Outline each blood parasite and name the species.
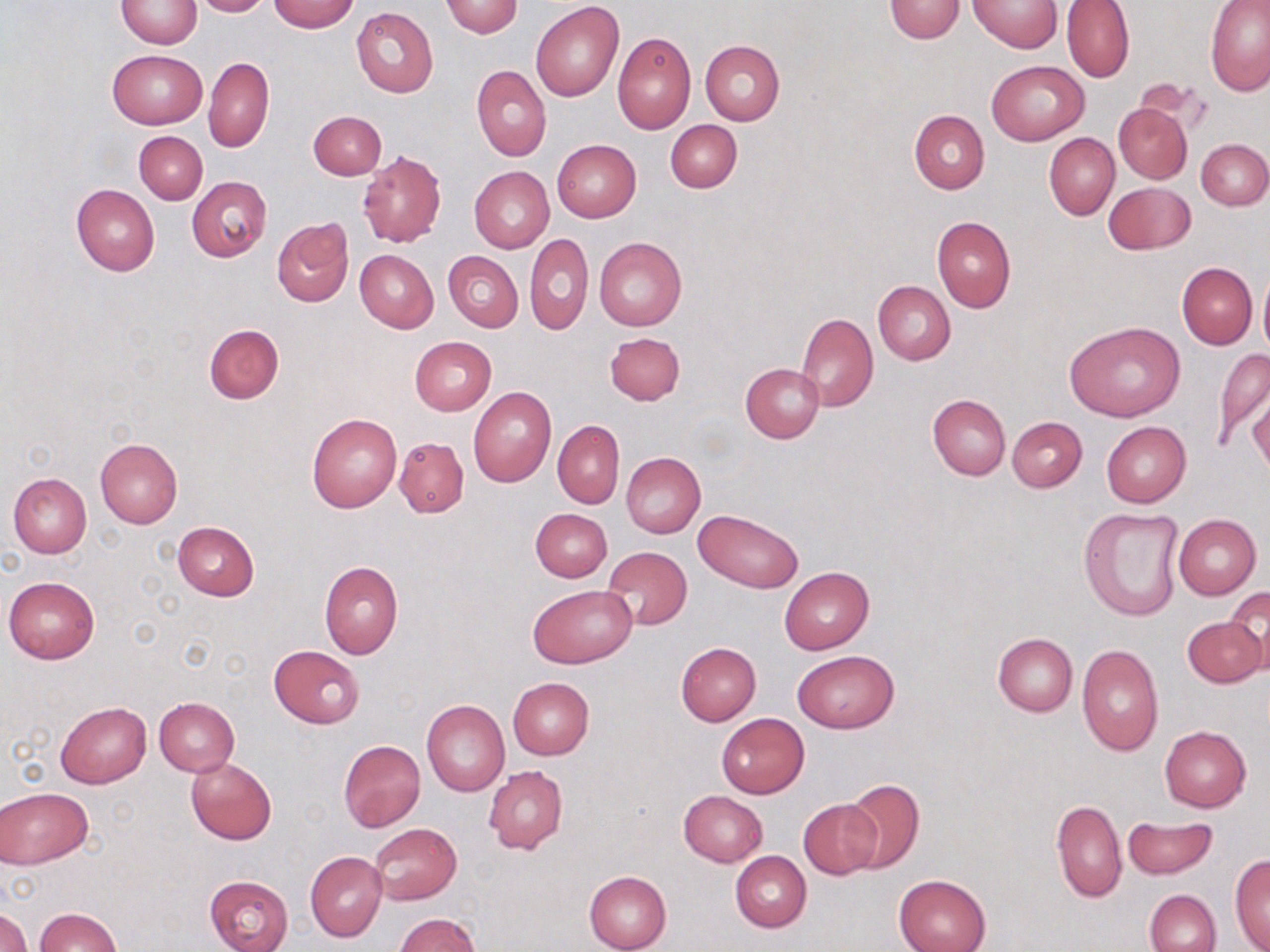
No blood parasites observed.

slide-level diagnosis = no evidence of blood parasites
image size = 1270×952 pixels
uninfected red blood cell locations = approximate bounding boxes as (x1,y1)-(x2,y2) corner pairs in pixels: (117,0)-(203,48), (192,0)-(270,17), (968,0)-(1062,52), (270,1)-(358,33), (440,1)-(523,38), (884,1)-(966,42), (1062,1)-(1136,83), (1205,2)-(1270,97), (531,3)-(623,101), (351,7)-(438,98), (612,32)-(696,133), (700,40)-(785,125), (107,49)-(207,129), (205,57)-(274,152), (985,59)-(1090,145), (472,66)-(551,161), (1114,103)-(1192,184), (308,110)-(385,180), (908,110)-(988,193), (665,119)-(741,192), (134,131)-(207,204), (1045,133)-(1119,219), (552,139)-(642,222), (1197,139)-(1270,210), (357,149)-(447,249), (469,166)-(554,253), (187,177)-(271,260), (1104,182)-(1194,254), (71,184)-(160,276), (932,216)-(1016,313), (272,218)-(354,307), (525,233)-(593,335), (594,236)-(687,330), (354,249)-(438,333), (443,250)-(523,332), (1177,262)-(1256,349), (1258,266)-(1270,360), (873,280)-(956,364), (796,313)-(878,410), (1066,323)-(1183,422), (204,324)-(284,403), (606,331)-(685,405), (409,337)-(496,415), (1211,346)-(1270,451), (740,363)-(823,443), (468,387)-(557,487), (1248,392)-(1270,475), (928,395)-(1010,480), (307,413)-(401,512), (1008,416)-(1087,492), (552,420)-(624,508), (1101,421)-(1190,508), (395,437)-(469,516), (95,438)-(182,528), (621,453)-(705,537), (8,473)-(92,558), (530,508)-(612,582), (1078,508)-(1187,623), (695,509)-(803,593), (1173,514)-(1261,600), (172,521)-(260,600), (603,546)-(693,630), (319,560)-(403,659), (780,566)-(874,654), (3,576)-(99,665), (528,585)-(635,669), (1227,587)-(1269,673), (1183,615)-(1266,689), (992,633)-(1078,717), (676,642)-(761,725), (1076,644)-(1163,757), (268,645)-(364,728), (791,650)-(899,734), (508,677)-(595,760), (152,696)-(239,777), (421,699)-(509,797), (55,702)-(152,788), (716,713)-(810,799), (1160,726)-(1251,812), (338,740)-(425,832), (186,757)-(277,844), (485,765)-(568,854), (841,779)-(925,873), (1,787)-(92,868), (678,790)-(768,867), (799,798)-(883,880), (1051,798)-(1126,903), (1121,816)-(1219,881), (370,822)-(461,905), (305,851)-(387,942), (731,851)-(811,932), (1230,854)-(1270,951), (583,870)-(673,952), (203,874)-(295,952), (894,874)-(991,952), (1144,889)-(1220,952), (1,907)-(33,952), (34,907)-(122,952), (397,913)-(480,952)
magnification = 1000x
preparation = thin blood smear
field of view = single
modality = light microscopy
stain = May-Grünwald-Giemsa